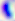
Toxoplasma gondii is shown. Photomicrograph. 400x magnification.